Report the malaria status of this cell.
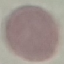
It is uninfected.

Summary:
  - Image type: automatically extracted cell patch, resized to 64 × 64 pixels
  - Preparation: thin smear
  - Capture: smartphone through the microscope eyepiece
  - Stain: Giemsa